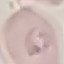

malaria status = parasitized
stain = Giemsa
capture = smartphone through the microscope eyepiece
image type = automatically extracted cell patch, resized to 64 × 64 pixels
preparation = thin blood film